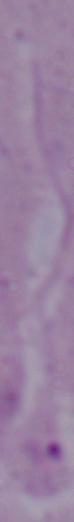

{
  "magnification": "1000x",
  "modality": "photomicrograph",
  "identification": "Leishmania"
}